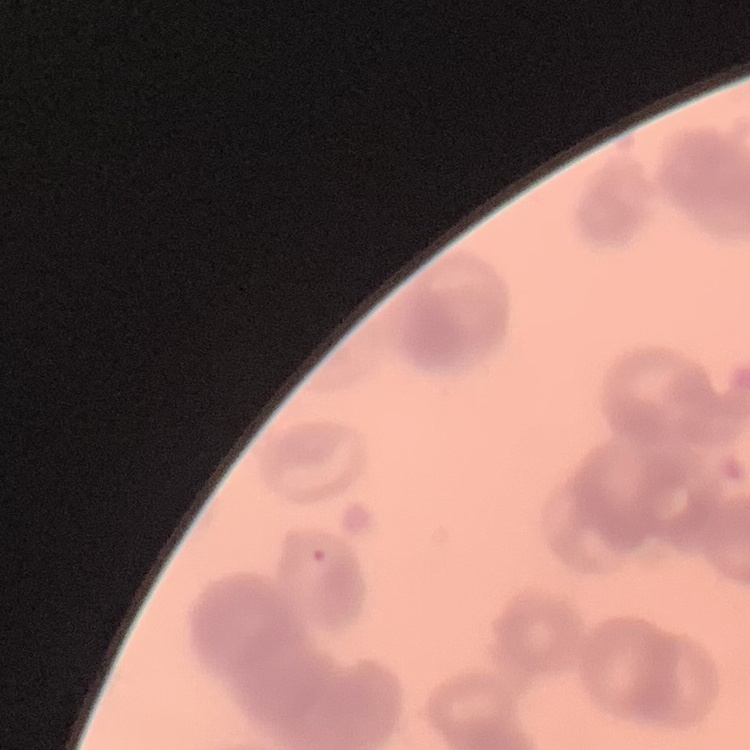
red blood cell morphology = rouleaux formation
image type = one tile cut from a larger photomicrograph
stain = Field's or Giemsa
preparation = thin peripheral smear